State which parasite is depicted.
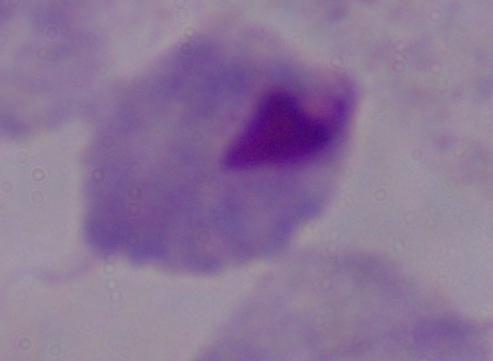

A trichomonad.

Summary:
  - Modality: photomicrograph
  - Magnification: 1000x